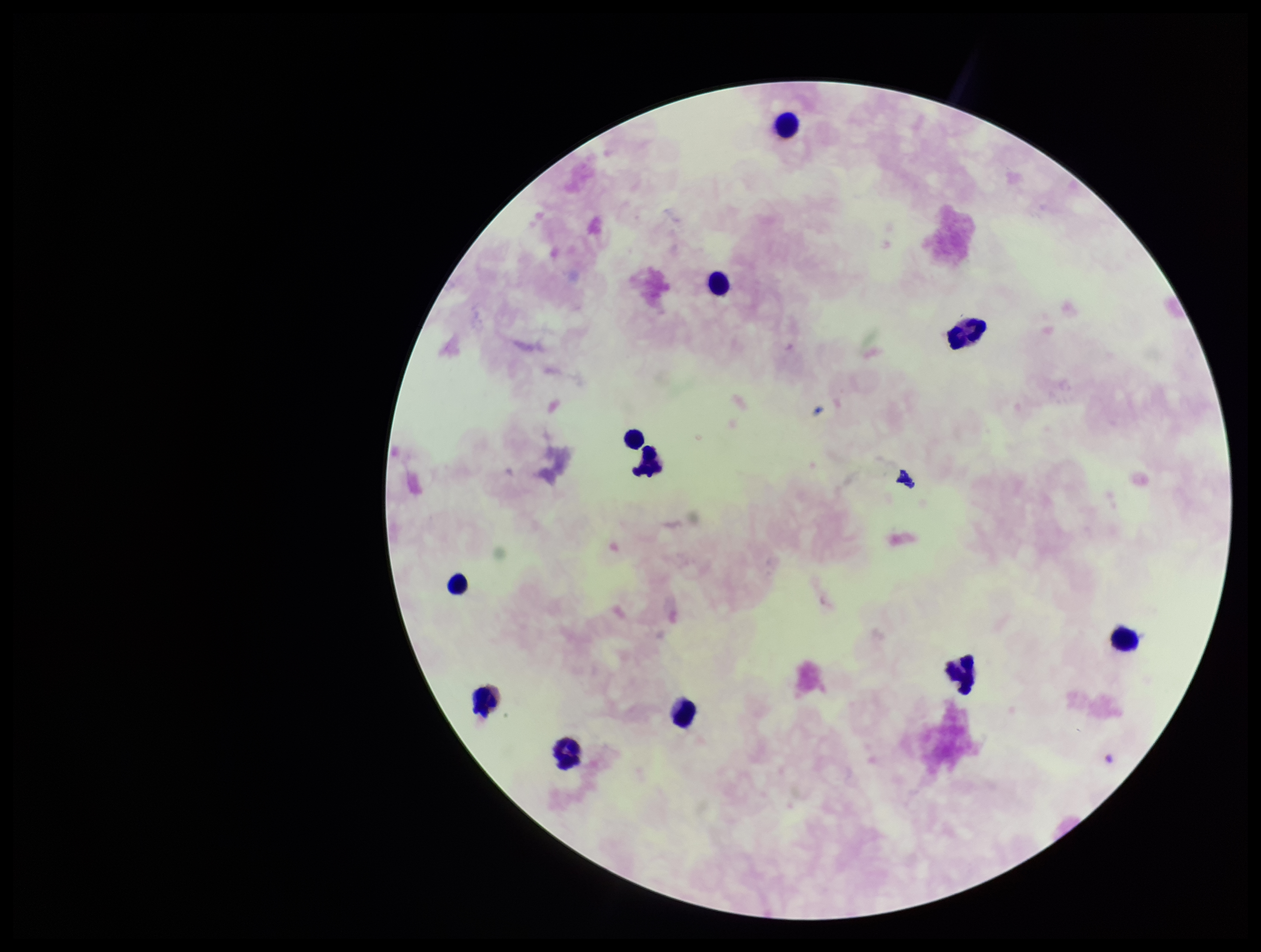
Leukocyte count: 11. Smartphone photograph taken through the eyepiece of a microscope. Image is 1261×952 pixels. Stained with Giemsa. Preparation: thick blood smear. Parasite count: 0. Single field of view. Patient malaria status: negative. Plasmodium parasites: none detected.